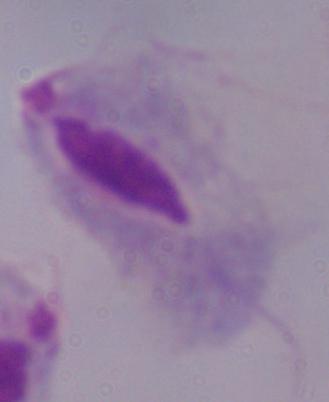
Summary:
  - Identification: trichomonad
  - Magnification: 1000x
  - Modality: photomicrograph